Identify the parasite.
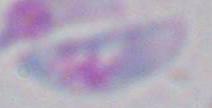

Toxoplasma gondii.

magnification: 1000x
modality: photomicrograph